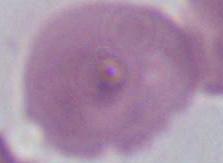

Photomicrograph. Captured at 1000x magnification. An erythrocyte is shown.